Name the blood parasite species.
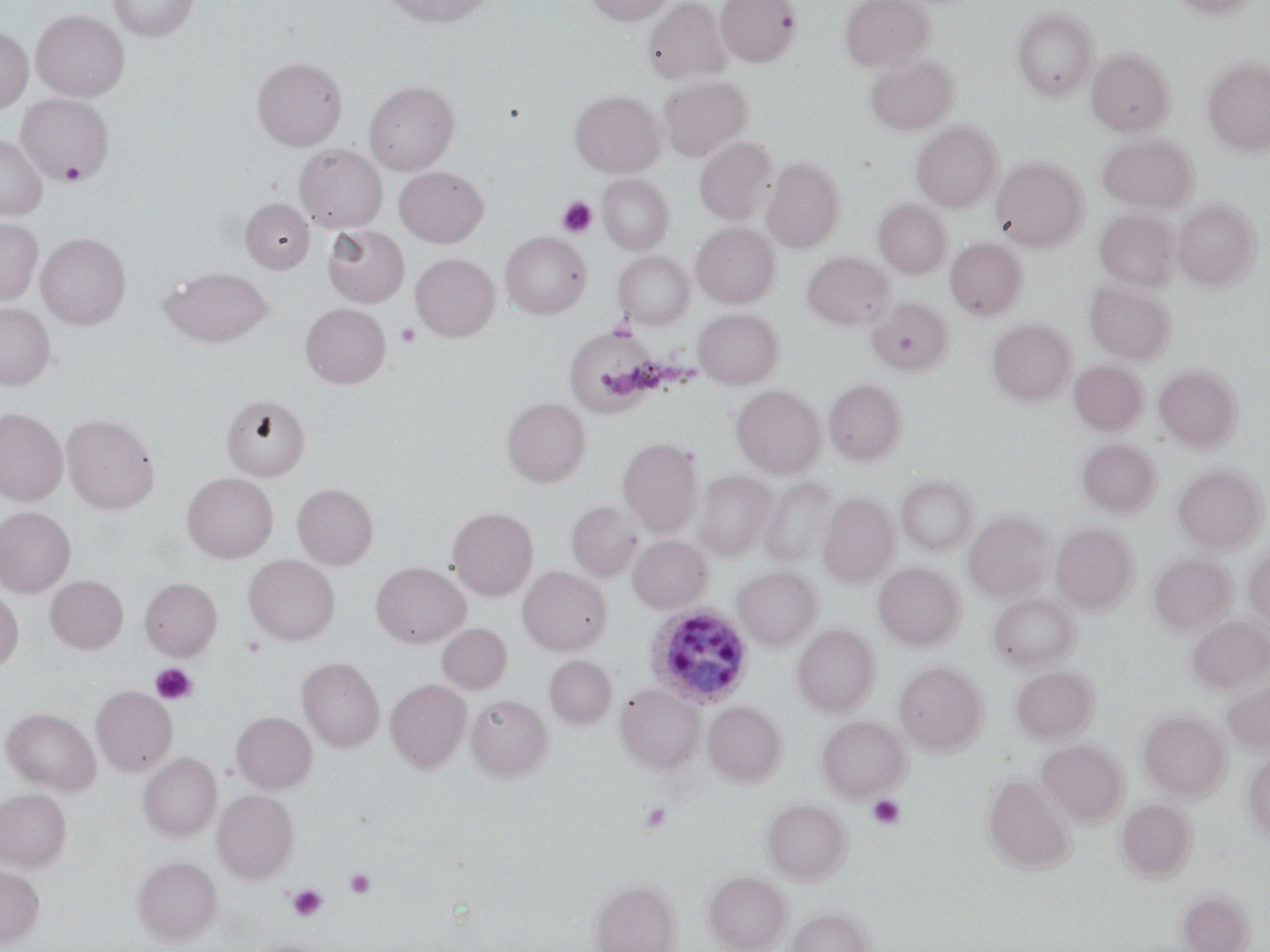

Plasmodium ovale.

Approximate bounding boxes as (x1, y1, x2, y2) in pixels. Plasmodium ovale-infected red blood cell locations: (646, 603, 754, 708). Platelet locations: (59, 159, 88, 184), (557, 196, 598, 237), (396, 323, 420, 347), (150, 663, 198, 705), (868, 794, 905, 829), (638, 801, 671, 834), (345, 869, 376, 899), (286, 884, 328, 921). Uninfected red blood cell locations: (107, 0, 199, 42), (381, 0, 496, 28), (583, 0, 675, 25), (642, 0, 731, 84), (715, 0, 801, 66), (840, 0, 933, 71), (1171, 0, 1258, 19), (1012, 7, 1099, 100), (31, 9, 129, 101), (0, 26, 33, 113), (1086, 48, 1174, 136), (865, 55, 957, 136), (1203, 56, 1270, 155), (252, 57, 347, 150), (658, 76, 752, 162), (365, 80, 460, 175), (570, 90, 664, 177), (16, 93, 114, 184), (911, 121, 1002, 212), (0, 134, 47, 220), (1097, 134, 1198, 213), (694, 136, 777, 225), (294, 144, 387, 233), (761, 157, 844, 252), (991, 157, 1087, 251), (394, 166, 489, 247), (597, 174, 673, 255), (240, 198, 314, 273), (1173, 198, 1261, 291), (873, 199, 951, 278), (1093, 209, 1179, 291), (0, 218, 42, 305), (691, 222, 780, 307), (323, 225, 410, 307), (501, 231, 591, 319), (36, 232, 131, 329), (945, 238, 1027, 321), (612, 251, 694, 329), (802, 252, 894, 329), (410, 253, 499, 341), (160, 266, 274, 347), (1084, 280, 1175, 364), (867, 297, 952, 375), (0, 303, 55, 389), (301, 303, 391, 388), (693, 308, 783, 388), (987, 319, 1076, 405), (565, 327, 664, 415), (1069, 360, 1146, 434), (1155, 366, 1242, 451), (824, 378, 906, 465), (731, 385, 825, 477), (222, 394, 310, 481), (502, 398, 590, 487), (0, 408, 68, 505), (62, 414, 159, 513), (618, 437, 704, 537), (1077, 438, 1160, 517), (1172, 464, 1267, 553), (693, 470, 776, 561), (182, 473, 278, 563), (896, 475, 978, 556), (759, 476, 837, 569), (292, 483, 378, 569), (818, 493, 899, 587), (567, 500, 643, 581), (0, 506, 76, 597), (448, 507, 538, 599), (964, 511, 1053, 601), (1051, 523, 1138, 613), (627, 535, 712, 613), (1244, 548, 1270, 628), (244, 554, 340, 645), (1149, 554, 1236, 636), (371, 562, 470, 648), (873, 562, 965, 650), (518, 566, 612, 655), (732, 566, 822, 651), (45, 575, 128, 654), (140, 577, 222, 660), (0, 587, 23, 672), (989, 593, 1079, 672), (1186, 615, 1270, 695), (437, 623, 511, 693), (792, 624, 880, 717), (544, 655, 616, 729), (297, 657, 384, 752), (894, 660, 987, 755), (1011, 666, 1099, 744), (1222, 677, 1269, 754), (385, 679, 471, 774), (615, 683, 704, 773), (91, 685, 178, 777), (466, 694, 552, 781), (704, 702, 786, 785), (2, 707, 100, 795), (1139, 709, 1230, 801), (231, 711, 317, 794), (817, 715, 910, 801), (1037, 739, 1129, 827), (138, 752, 222, 842), (1243, 753, 1270, 841), (983, 773, 1077, 875), (0, 788, 71, 872), (212, 788, 299, 883), (762, 798, 852, 884), (1116, 798, 1197, 881), (131, 855, 223, 946), (0, 864, 45, 947), (703, 870, 791, 952), (590, 879, 681, 952), (1178, 889, 1254, 952), (787, 906, 875, 952), (246, 939, 334, 952). Optical microscopy. Thin blood smear. One field of a larger specimen. Image is 1270×952 pixels. May-Grünwald-Giemsa stain. 1000x magnification.